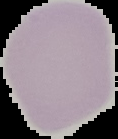
Image is 118×139 pixels. Segmented cell region on a black background. Malaria status: uninfected. From a thin blood smear.